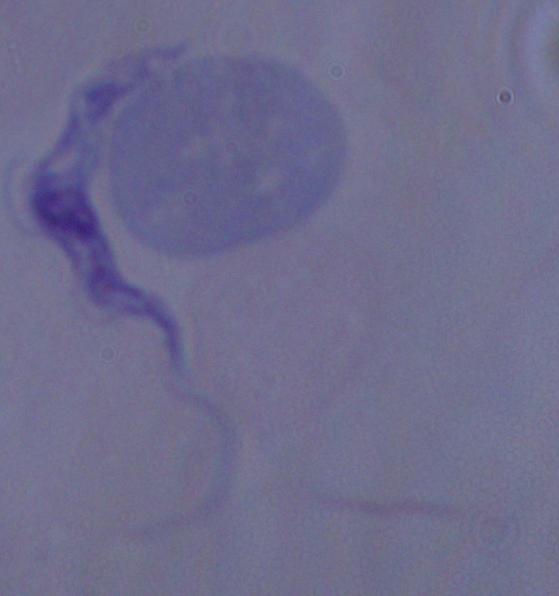
identification = trypanosome
modality = photomicrograph
magnification = 1000x